Outline each Plasmodium falciparum-infected red blood cell.
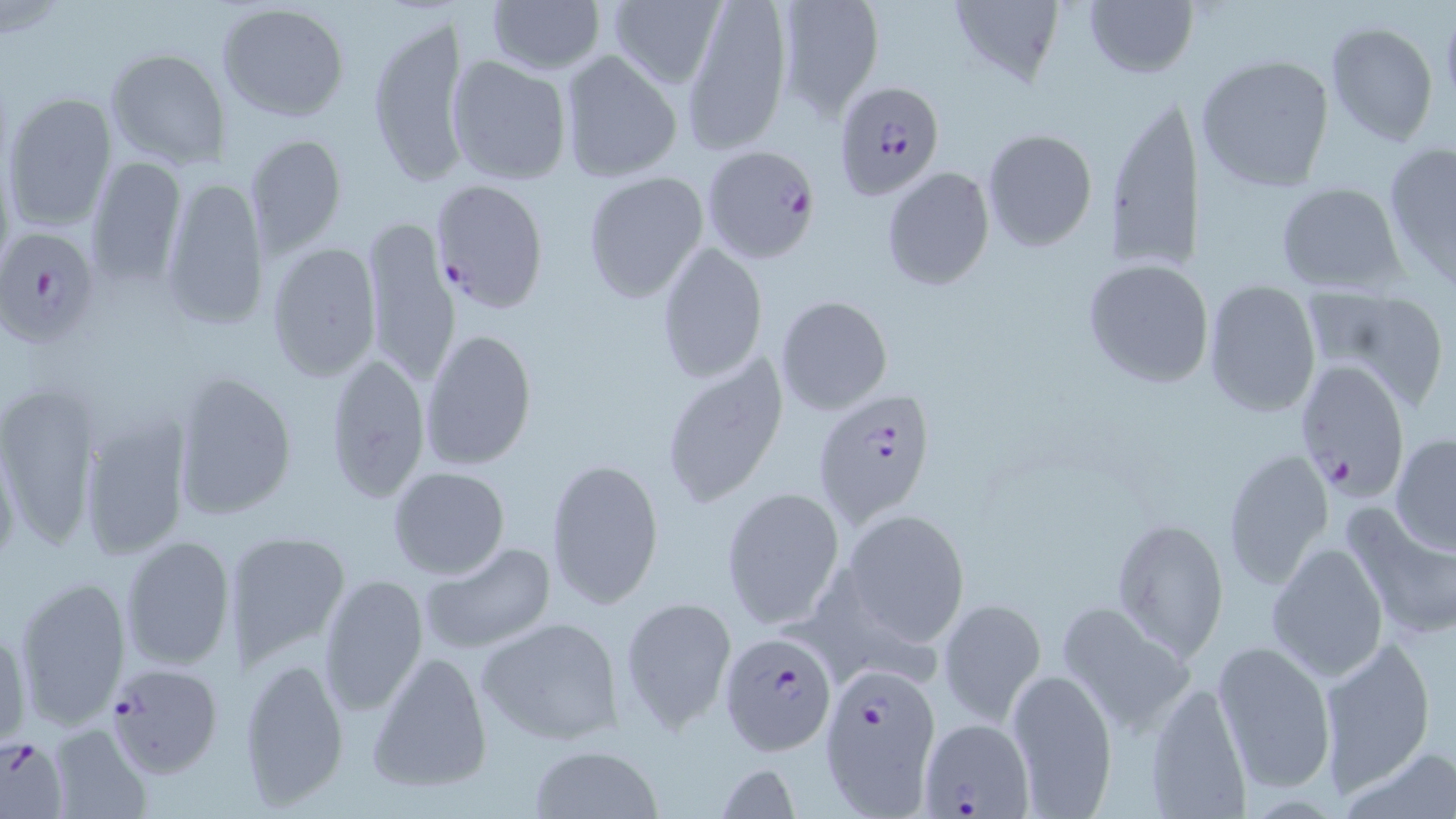
Approximate bounding boxes as named x1/y1/x2/y2 corners in pixels.
Plasmodium falciparum-infected red blood cells: (x1=833, y1=80, x2=946, y2=200), (x1=701, y1=144, x2=823, y2=268), (x1=432, y1=178, x2=550, y2=314), (x1=0, y1=226, x2=104, y2=351), (x1=1291, y1=350, x2=1415, y2=502), (x1=814, y1=389, x2=938, y2=526), (x1=719, y1=634, x2=839, y2=757), (x1=105, y1=661, x2=227, y2=778), (x1=819, y1=661, x2=941, y2=809), (x1=918, y1=713, x2=1035, y2=816), (x1=0, y1=733, x2=70, y2=819).

Uninfected red blood cell locations: (x1=486, y1=0, x2=606, y2=75), (x1=606, y1=0, x2=725, y2=90), (x1=682, y1=0, x2=793, y2=153), (x1=946, y1=0, x2=1068, y2=90), (x1=773, y1=1, x2=884, y2=122), (x1=1083, y1=1, x2=1196, y2=79), (x1=217, y1=2, x2=350, y2=120), (x1=367, y1=10, x2=467, y2=190), (x1=1324, y1=20, x2=1441, y2=147), (x1=104, y1=47, x2=229, y2=171), (x1=558, y1=49, x2=684, y2=183), (x1=1194, y1=53, x2=1337, y2=193), (x1=446, y1=55, x2=572, y2=186), (x1=4, y1=90, x2=118, y2=231), (x1=1101, y1=92, x2=1201, y2=277), (x1=980, y1=128, x2=1099, y2=251), (x1=244, y1=132, x2=347, y2=257), (x1=1382, y1=141, x2=1456, y2=290), (x1=85, y1=157, x2=188, y2=287), (x1=881, y1=165, x2=995, y2=293), (x1=582, y1=170, x2=710, y2=303), (x1=158, y1=173, x2=270, y2=332), (x1=1273, y1=180, x2=1406, y2=296), (x1=361, y1=215, x2=460, y2=389), (x1=266, y1=242, x2=381, y2=381), (x1=656, y1=242, x2=769, y2=383), (x1=1083, y1=260, x2=1216, y2=388), (x1=1202, y1=283, x2=1321, y2=417), (x1=1301, y1=288, x2=1447, y2=411), (x1=774, y1=295, x2=892, y2=416), (x1=421, y1=326, x2=538, y2=474), (x1=658, y1=350, x2=789, y2=509), (x1=320, y1=353, x2=431, y2=503), (x1=171, y1=371, x2=298, y2=523), (x1=0, y1=381, x2=99, y2=552), (x1=80, y1=413, x2=192, y2=559), (x1=1390, y1=433, x2=1456, y2=554), (x1=0, y1=437, x2=22, y2=572), (x1=1222, y1=447, x2=1334, y2=589), (x1=544, y1=457, x2=665, y2=612), (x1=388, y1=465, x2=510, y2=580), (x1=721, y1=488, x2=844, y2=630), (x1=1342, y1=504, x2=1456, y2=642), (x1=844, y1=509, x2=970, y2=646), (x1=1112, y1=519, x2=1226, y2=661), (x1=222, y1=531, x2=350, y2=663), (x1=120, y1=535, x2=237, y2=672), (x1=1266, y1=541, x2=1389, y2=681), (x1=420, y1=542, x2=558, y2=656), (x1=315, y1=571, x2=429, y2=716), (x1=13, y1=575, x2=134, y2=730), (x1=621, y1=596, x2=737, y2=734), (x1=937, y1=598, x2=1047, y2=725), (x1=1057, y1=601, x2=1198, y2=733), (x1=475, y1=615, x2=628, y2=747), (x1=1, y1=618, x2=30, y2=747), (x1=1210, y1=637, x2=1338, y2=793), (x1=1317, y1=637, x2=1435, y2=792), (x1=366, y1=652, x2=493, y2=793), (x1=238, y1=653, x2=351, y2=809), (x1=1006, y1=667, x2=1118, y2=817), (x1=1144, y1=679, x2=1255, y2=818), (x1=47, y1=723, x2=151, y2=818), (x1=529, y1=744, x2=662, y2=819), (x1=1344, y1=744, x2=1452, y2=819), (x1=712, y1=763, x2=801, y2=818). Slide-level diagnosis: Plasmodium falciparum. Image is 1456×819 pixels. Captured at 1000x magnification. Single field of view. May-Grünwald-Giemsa stain. Thin blood smear. Light microscopy.